Outline each blood parasite and name the species.
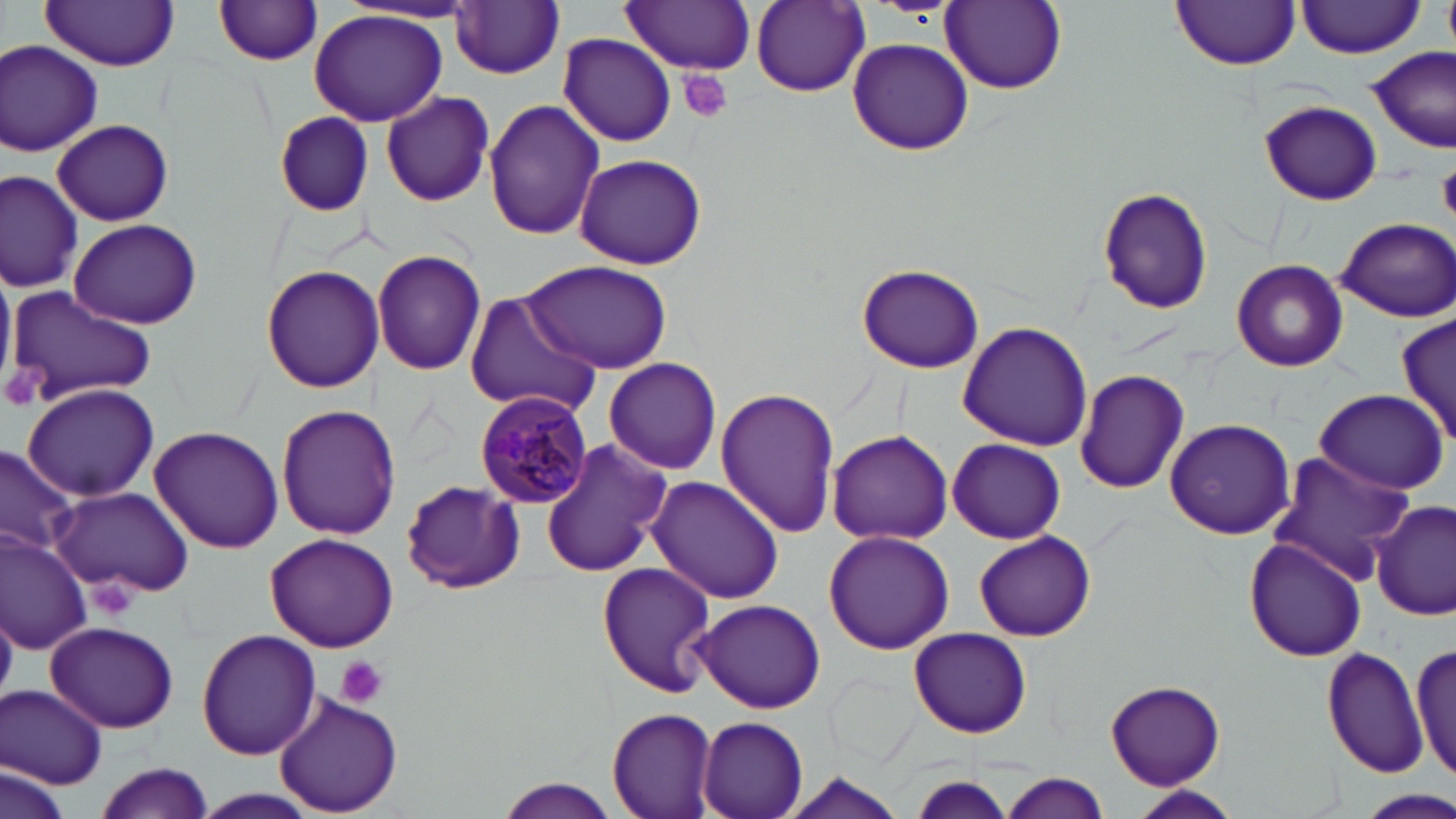
Approximate bounding boxes as named x1/y1/x2/y2 corners in pixels.
Plasmodium malariae-infected red blood cells: (x1=476, y1=392, x2=595, y2=510).
No Plasmodium falciparum, Plasmodium ovale, Plasmodium vivax, Babesia divergens, or Trypanosoma brucei observed.

Uninfected red blood cell locations: (x1=621, y1=0, x2=756, y2=73), (x1=940, y1=0, x2=1067, y2=93), (x1=212, y1=1, x2=326, y2=66), (x1=751, y1=1, x2=869, y2=96), (x1=1170, y1=1, x2=1301, y2=71), (x1=1296, y1=1, x2=1424, y2=57), (x1=451, y1=2, x2=565, y2=78), (x1=40, y1=3, x2=181, y2=69), (x1=308, y1=10, x2=447, y2=127), (x1=558, y1=34, x2=676, y2=148), (x1=847, y1=37, x2=973, y2=157), (x1=0, y1=39, x2=103, y2=157), (x1=1365, y1=47, x2=1455, y2=154), (x1=381, y1=92, x2=495, y2=207), (x1=483, y1=98, x2=605, y2=239), (x1=1257, y1=99, x2=1383, y2=206), (x1=269, y1=111, x2=376, y2=215), (x1=53, y1=119, x2=173, y2=226), (x1=575, y1=154, x2=706, y2=270), (x1=1, y1=171, x2=82, y2=293), (x1=1093, y1=186, x2=1215, y2=318), (x1=68, y1=217, x2=203, y2=330), (x1=1336, y1=217, x2=1456, y2=322), (x1=372, y1=248, x2=485, y2=376), (x1=520, y1=258, x2=670, y2=372), (x1=1231, y1=258, x2=1349, y2=372), (x1=0, y1=262, x2=15, y2=392), (x1=855, y1=262, x2=985, y2=374), (x1=260, y1=264, x2=383, y2=393), (x1=4, y1=287, x2=156, y2=411), (x1=464, y1=294, x2=600, y2=416), (x1=1399, y1=314, x2=1456, y2=448), (x1=957, y1=320, x2=1095, y2=451), (x1=605, y1=358, x2=721, y2=474), (x1=1074, y1=369, x2=1190, y2=495), (x1=21, y1=383, x2=159, y2=503), (x1=715, y1=386, x2=840, y2=538), (x1=1312, y1=388, x2=1449, y2=491), (x1=277, y1=404, x2=401, y2=540), (x1=1164, y1=417, x2=1296, y2=538), (x1=149, y1=425, x2=284, y2=554), (x1=827, y1=429, x2=954, y2=544), (x1=948, y1=438, x2=1066, y2=544), (x1=539, y1=439, x2=671, y2=578), (x1=0, y1=443, x2=80, y2=560), (x1=1263, y1=451, x2=1422, y2=585), (x1=400, y1=477, x2=523, y2=596), (x1=647, y1=477, x2=785, y2=607), (x1=50, y1=486, x2=194, y2=598), (x1=1372, y1=498, x2=1455, y2=621), (x1=824, y1=530, x2=954, y2=653), (x1=973, y1=530, x2=1095, y2=641), (x1=0, y1=533, x2=91, y2=654), (x1=264, y1=533, x2=402, y2=653), (x1=1244, y1=536, x2=1367, y2=663), (x1=595, y1=561, x2=719, y2=700), (x1=690, y1=601, x2=827, y2=713), (x1=45, y1=621, x2=180, y2=734), (x1=909, y1=627, x2=1032, y2=739), (x1=196, y1=629, x2=322, y2=761), (x1=1412, y1=639, x2=1455, y2=787), (x1=1322, y1=647, x2=1427, y2=776), (x1=1104, y1=680, x2=1225, y2=789), (x1=2, y1=685, x2=108, y2=789), (x1=271, y1=693, x2=405, y2=817), (x1=607, y1=707, x2=720, y2=819), (x1=696, y1=714, x2=810, y2=819), (x1=95, y1=761, x2=217, y2=817), (x1=3, y1=763, x2=69, y2=819), (x1=780, y1=770, x2=913, y2=819), (x1=999, y1=772, x2=1111, y2=819), (x1=905, y1=776, x2=1019, y2=818), (x1=492, y1=778, x2=626, y2=818), (x1=1123, y1=785, x2=1243, y2=819), (x1=186, y1=788, x2=325, y2=818), (x1=1360, y1=790, x2=1454, y2=818). Platelet locations: (x1=678, y1=69, x2=733, y2=124), (x1=1438, y1=166, x2=1456, y2=220), (x1=335, y1=656, x2=386, y2=709). Slide-level diagnosis: Plasmodium malariae. 1000x magnification. Image is 1456×819 pixels. One field of a larger specimen. Optical microscopy. May-Grünwald-Giemsa stain. Thin blood film.